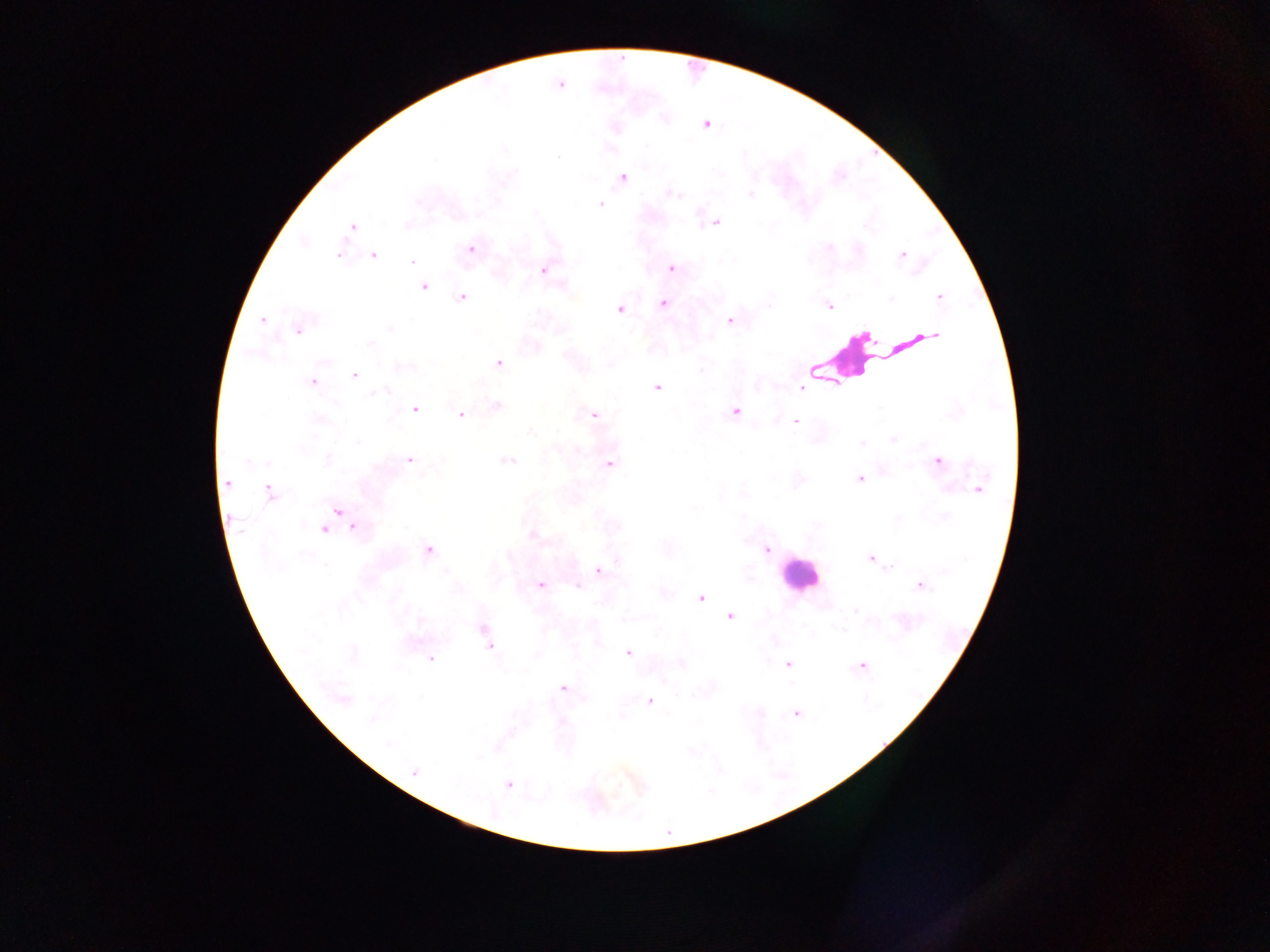

Approximate centers as [x, y] in pixels. Leukocyte locations: [859, 360], [798, 574]. Malaria parasite locations: [706, 125], [557, 157], [623, 177], [673, 193], [750, 194], [600, 204], [715, 223], [353, 227], [304, 242], [471, 248], [339, 254], [902, 255], [373, 256], [413, 262], [671, 269], [543, 271], [424, 288], [939, 297], [462, 298], [891, 299], [663, 304], [829, 306], [620, 309], [262, 319], [729, 321], [390, 327], [298, 331], [934, 336], [371, 344], [499, 363], [404, 367], [700, 371], [354, 375], [312, 382], [801, 387], [656, 388], [384, 390], [375, 392], [497, 405], [878, 408], [415, 410], [735, 412], [594, 414], [461, 415], [320, 420], [795, 422], [531, 432], [893, 439], [358, 443], [861, 444], [328, 460], [410, 460], [507, 461], [937, 461], [610, 464], [860, 479], [228, 483], [978, 490], [269, 491], [338, 511], [945, 517], [354, 527], [323, 530], [533, 535], [429, 550], [766, 550], [870, 558], [326, 565], [891, 567], [599, 570], [446, 572], [540, 585], [920, 585], [578, 586], [701, 597], [856, 610], [729, 617], [484, 632], [488, 645], [627, 652], [430, 659], [787, 664], [862, 666], [563, 688], [344, 700], [650, 701], [796, 714], [372, 719], [388, 745], [414, 772], [508, 785]. Sample from Ghana. Image is 1270×952 pixels. One field of view. Photographed through a microscope with a mobile-phone camera. Thick blood film.